Classify this cell by malaria status.
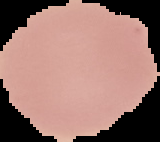

It is uninfected.

Image is 160×142 pixels. Cell region segmented out of the field of view; the surrounding area is masked to black. From a thin blood film.